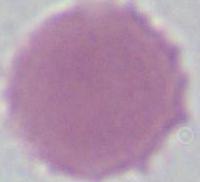

Summary:
  - Modality: photomicrograph
  - Magnification: 1000x
  - Identification: erythrocyte